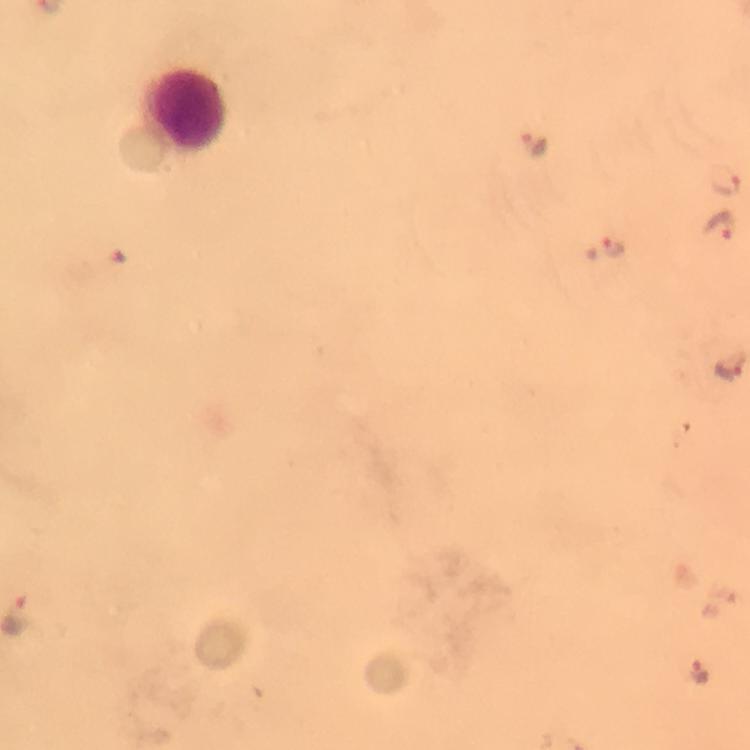

capture = smartphone mounted on the microscope
malaria parasite locations = approximate centers as {x, y} in pixels: {536, 141}, {724, 181}, {719, 226}, {614, 246}, {702, 673}
preparation = thick smear
image size = 750×750 pixels
stain = Giemsa
immersion oil = applied
leukocyte locations = approximate centers as {x, y} in pixels: {188, 109}
cropped from = a single field of view
context = from a diagnostic examination for malaria
magnification = 100x